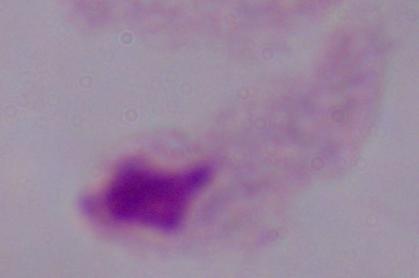

identification = trichomonad
modality = photomicrograph
magnification = 1000x